Assess this cell for malaria.
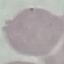

It is uninfected.

Summary:
  - Preparation: thin blood smear
  - Capture: smartphone camera at the microscope eyepiece
  - Image type: automatically extracted cell patch, resized to 64 × 64 pixels
  - Stain: Giemsa